Classify this cell by malaria status.
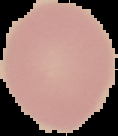
Uninfected.

{
  "image_size": "118×136 pixels",
  "preparation": "thin blood smear",
  "image_type": "cell region segmented out of the field of view; surrounding area masked to black"
}